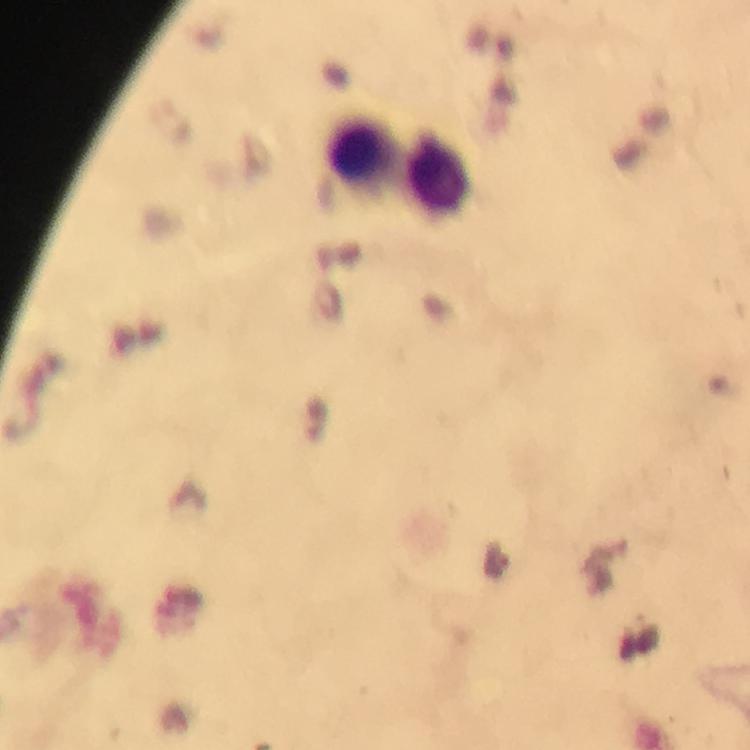

Approximate centers as {x, y} in pixels.
Summary:
  - Leukocyte locations: {360, 154}, {437, 177}
  - Image size: 750×750 pixels
  - Magnification: 100x
  - Context: from a malaria diagnostic workup
  - Cropped from: one field of view
  - Immersion oil: used
  - Capture: smartphone camera through the microscope
  - Stain: Giemsa
  - Plasmodium parasites: none seen
  - Preparation: thick blood smear